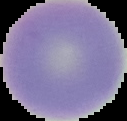
Cell region segmented out of the field of view; the surrounding area is masked to black. Result: negative for Plasmodium parasites. Image is 127×121 pixels. From a thin blood smear.